Comment on the morphology of the erythrocytes.
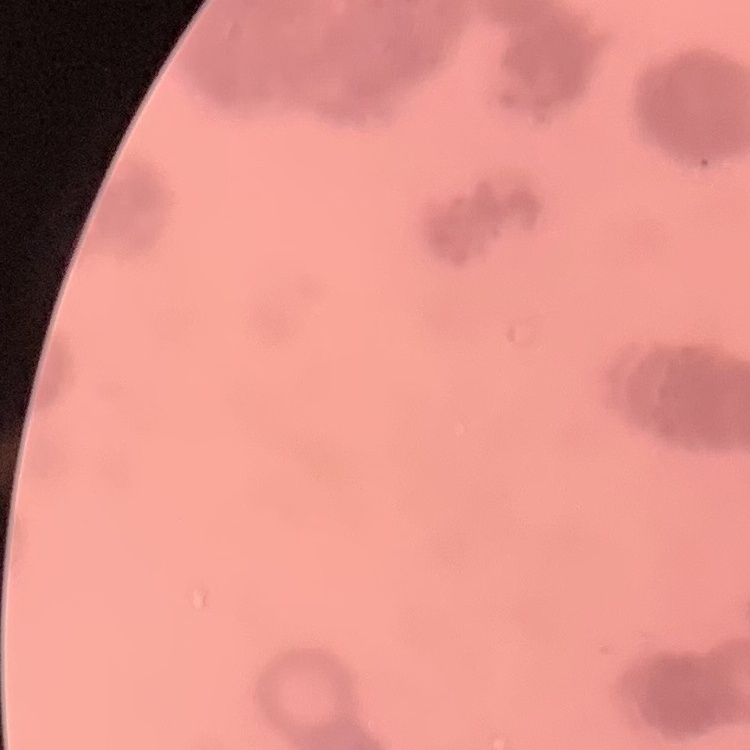
They show rouleaux formation.

One tile cut from a larger photomicrograph. Field's or Giemsa stain. Thin peripheral smear.